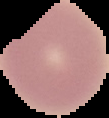
malaria status = uninfected
image size = 109×118 pixels
preparation = thin blood film
image type = cell region segmented out of the field of view; surrounding area masked to black